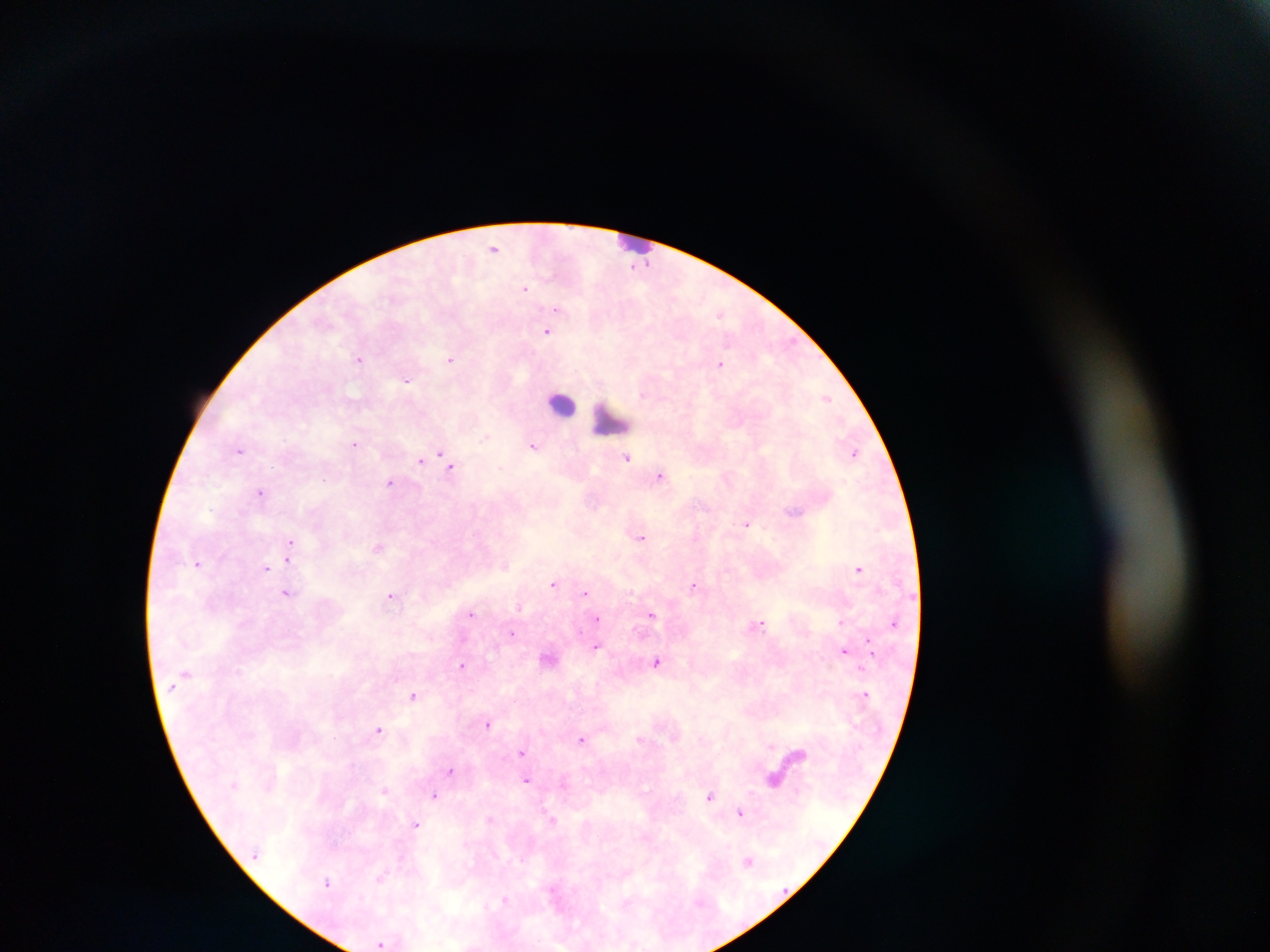
Approximate centers as (x, y) in pixels.
Summary:
  - Leukocyte locations: (631, 236), (562, 402), (608, 422)
  - Malaria parasite locations: (494, 247), (645, 261), (525, 288), (555, 309), (720, 314), (547, 331), (451, 358), (359, 360), (721, 364), (407, 381), (642, 394), (826, 398), (485, 437), (354, 444), (534, 447), (239, 450), (855, 452), (441, 454), (628, 458), (420, 460), (446, 460), (450, 467), (659, 476), (324, 478), (390, 482), (261, 493), (747, 524), (641, 537), (291, 542), (377, 547), (289, 556), (198, 564), (266, 567), (858, 569), (553, 584), (693, 585), (287, 593), (585, 593), (390, 597), (520, 607), (470, 614), (651, 615), (597, 618), (841, 622), (894, 623), (760, 624), (512, 633), (868, 644), (595, 647), (844, 651), (657, 662), (462, 665), (865, 695), (413, 696), (488, 724), (379, 729), (582, 739), (769, 745), (522, 751), (452, 770), (526, 780), (773, 781), (385, 790), (435, 794), (710, 796), (741, 813), (490, 819), (553, 820), (416, 824), (748, 861), (381, 876), (328, 882), (505, 900), (380, 944)
  - Field of view: single
  - Country: Ghana
  - Capture: mobile-phone photograph through a microscope
  - Preparation: thick blood smear
  - Image size: 1270×952 pixels